Assess this cell for malaria.
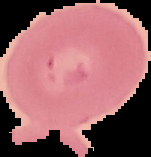

It is uninfected.

Image is 151×157 pixels. From a thin blood smear. The area outside the segmented cell region is set to black.